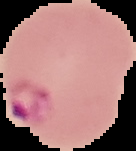

Summary:
  - Image size: 136×151 pixels
  - Image type: segmented cell region with the area outside set to black
  - Preparation: thin blood film
  - Malaria status: parasitized